Assess this cell for malaria.
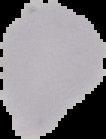

It is uninfected.

Cell region segmented out of the field of view; the surrounding area is masked to black. From a thin blood smear. Image is 106×139 pixels.